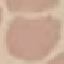

Summary:
  - Result: no malaria parasites detected
  - Capture: smartphone camera at the microscope eyepiece
  - Image type: automatically extracted cell patch, resized to 64 × 64 pixels
  - Stain: Giemsa
  - Preparation: thin blood film